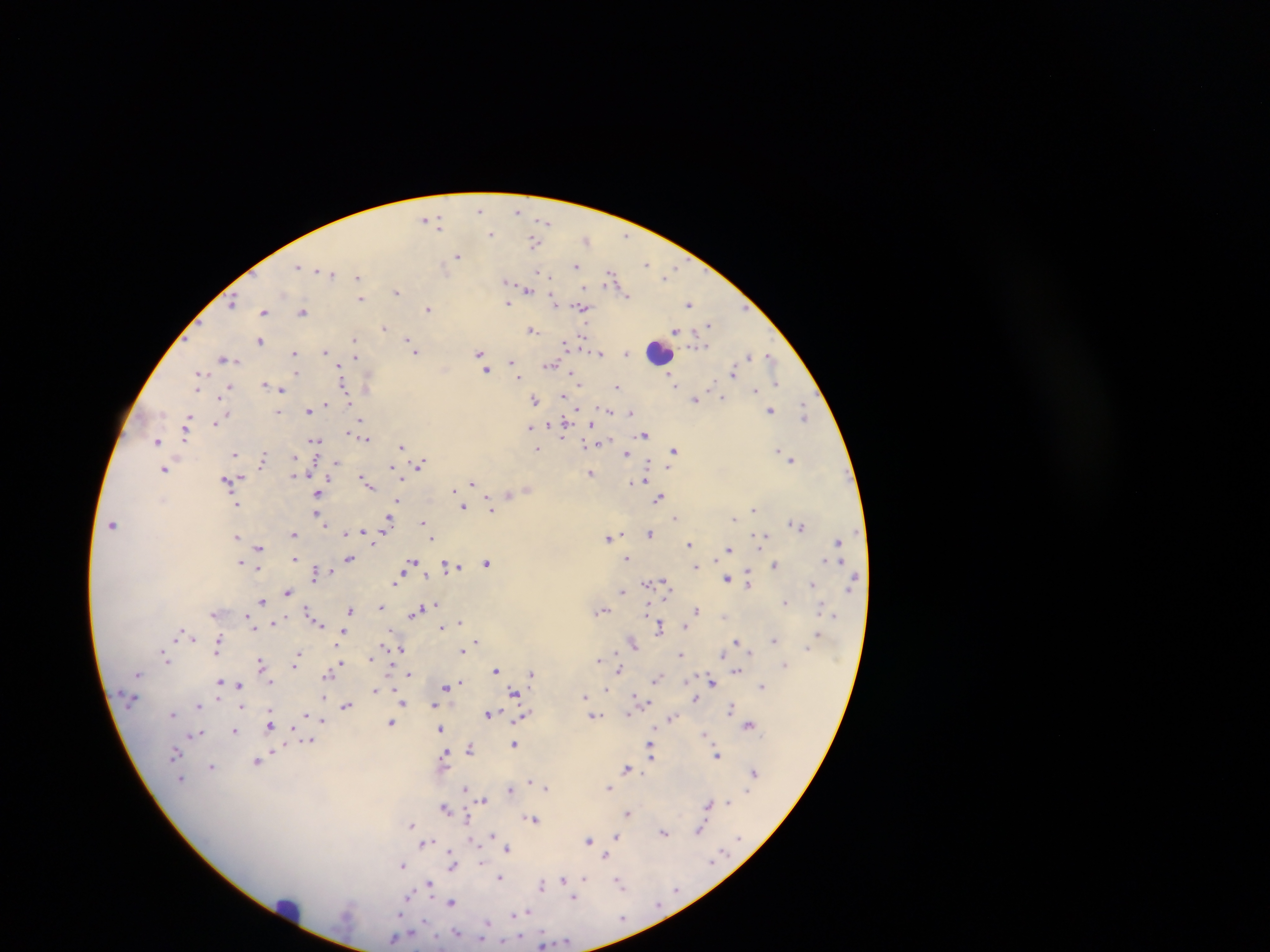 Approximate centers as [x, y] in pixels. Leukocyte locations: [660, 352], [287, 909]. Plasmodium parasite locations: [481, 208], [518, 210], [427, 218], [437, 220], [546, 222], [490, 234], [625, 236], [586, 240], [534, 242], [457, 255], [576, 264], [647, 264], [299, 268], [673, 269], [319, 270], [329, 273], [537, 273], [666, 276], [358, 277], [612, 278], [507, 281], [528, 289], [398, 291], [626, 295], [361, 299], [554, 300], [233, 301], [509, 302], [689, 304], [583, 307], [429, 308], [745, 308], [304, 310], [266, 311], [709, 326], [385, 328], [676, 330], [532, 331], [354, 339], [409, 339], [260, 340], [566, 344], [698, 344], [325, 351], [415, 351], [480, 352], [600, 353], [626, 353], [294, 354], [749, 355], [355, 356], [770, 357], [224, 358], [512, 360], [484, 362], [550, 366], [487, 369], [734, 372], [200, 374], [297, 374], [519, 376], [673, 380], [368, 382], [775, 382], [264, 386], [617, 387], [229, 388], [344, 388], [282, 389], [756, 390], [564, 396], [723, 397], [695, 398], [535, 400], [328, 402], [577, 409], [309, 410], [609, 410], [771, 410], [278, 411], [632, 412], [804, 413], [221, 418], [361, 419], [188, 420], [215, 422], [550, 424], [565, 424], [591, 425], [531, 427], [186, 428], [349, 433], [644, 434], [365, 438], [315, 439], [157, 442], [585, 443], [596, 443], [402, 446], [537, 449], [674, 450], [779, 450], [628, 453], [235, 455], [296, 457], [263, 459], [791, 459], [336, 464], [419, 465], [391, 466], [165, 469], [591, 472], [295, 474], [647, 478], [235, 479], [227, 480], [330, 480], [400, 482], [634, 482], [366, 483], [472, 483], [527, 488], [455, 489], [318, 494], [509, 494], [660, 496], [398, 499], [235, 503], [463, 507], [491, 508], [753, 510], [317, 514], [675, 518], [735, 518], [390, 519], [423, 522], [113, 524], [798, 525], [364, 532], [346, 533], [650, 533], [294, 534], [764, 534], [621, 535], [236, 537], [433, 537], [608, 537], [374, 540], [838, 541], [689, 543], [258, 548], [729, 549], [295, 557], [627, 559], [825, 559], [348, 560], [241, 561], [412, 561], [841, 561], [488, 563], [775, 564], [451, 566], [259, 567], [458, 567], [695, 567], [402, 571], [316, 572], [425, 572], [400, 576], [855, 577], [728, 578], [749, 579], [648, 582], [812, 582], [664, 583], [622, 590], [288, 591], [262, 599], [785, 602], [821, 606], [381, 607], [427, 608], [649, 608], [350, 609], [603, 609], [696, 609], [416, 610], [307, 611], [214, 614], [835, 614], [726, 615], [248, 616], [459, 622], [274, 623], [318, 623], [446, 626], [660, 626], [442, 627], [181, 633], [343, 633], [818, 633], [192, 637], [773, 639], [475, 640], [736, 641], [633, 643], [218, 645], [807, 647], [392, 648], [399, 648], [462, 650], [751, 650], [217, 654], [615, 654], [680, 654], [723, 654], [166, 657], [297, 657], [371, 658], [598, 660], [262, 663], [296, 663], [784, 664], [339, 665], [496, 668], [619, 670], [737, 670], [410, 673], [531, 674], [328, 675], [658, 679], [460, 680], [220, 681], [271, 682], [712, 682], [239, 685], [448, 685], [762, 686], [605, 689], [375, 690], [514, 692], [634, 695], [323, 696], [584, 696], [695, 697], [642, 698], [647, 701], [403, 702], [435, 703], [199, 705], [346, 705], [242, 706], [731, 707], [271, 710], [173, 713], [489, 713], [628, 713], [305, 714], [520, 716], [592, 716], [672, 717], [322, 719], [391, 722], [749, 724], [270, 725], [440, 728], [235, 730], [201, 732], [704, 733], [312, 740], [514, 743], [651, 743], [470, 748], [274, 749], [651, 752], [176, 753], [717, 754], [445, 755], [257, 761], [212, 765], [627, 769], [754, 773], [529, 780], [546, 787], [609, 787], [465, 789], [511, 789], [483, 800], [727, 803], [709, 804], [445, 807], [628, 812], [467, 817], [534, 819], [411, 823], [700, 829], [664, 832], [493, 835], [615, 835], [474, 839], [589, 840], [425, 843], [508, 848], [451, 854], [607, 854], [452, 861], [482, 862], [403, 864], [452, 868], [500, 876], [584, 876], [564, 879], [619, 882], [429, 884], [542, 886], [575, 896], [411, 897], [451, 902], [528, 911], [402, 915], [513, 915], [488, 922], [457, 932], [394, 937], [481, 939], [503, 941]. Thick blood film. Photographed through a microscope with a mobile-phone camera. Sample from Ghana. Single field of view. Image is 1270×952 pixels.